Outline each blood parasite and name the species.
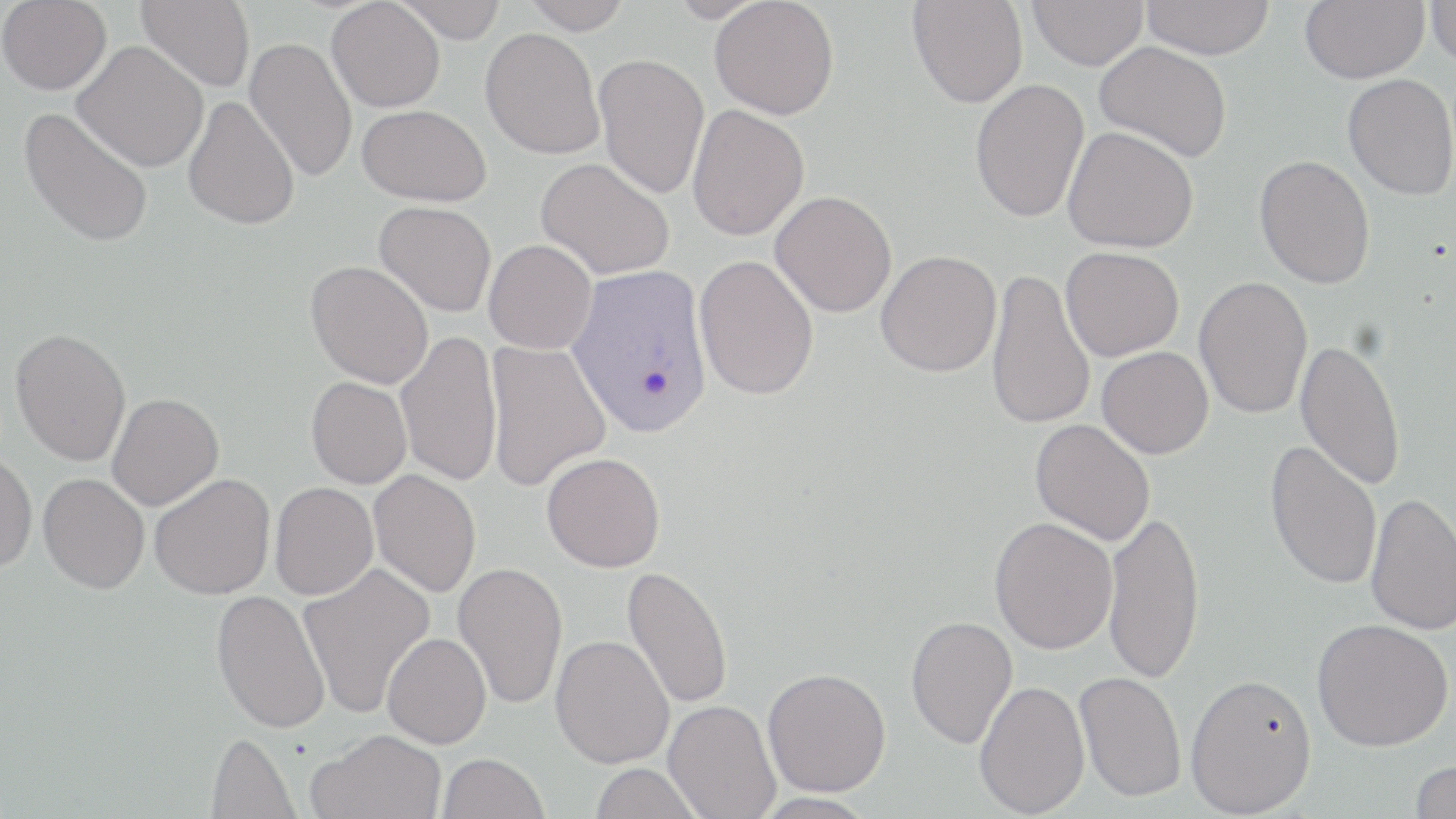

Approximate bounding boxes as (x1, y1, x2, y2) in pixels.
Plasmodium vivax-infected red blood cells: (567, 264, 713, 436).
No Plasmodium falciparum, Plasmodium ovale, Plasmodium malariae, Babesia divergens, or Trypanosoma brucei observed.

Uninfected red blood cell locations: (0, 0, 111, 95), (136, 0, 255, 92), (392, 0, 508, 42), (522, 0, 633, 34), (667, 0, 771, 23), (710, 0, 839, 119), (1028, 0, 1149, 70), (1140, 0, 1275, 59), (1300, 0, 1429, 83), (1425, 0, 1456, 68), (327, 1, 445, 112), (908, 1, 1028, 108), (480, 27, 605, 160), (244, 37, 357, 183), (73, 40, 209, 172), (1094, 42, 1232, 162), (594, 53, 709, 199), (1343, 74, 1456, 200), (970, 79, 1089, 223), (182, 95, 300, 230), (687, 104, 810, 241), (357, 105, 491, 205), (19, 106, 154, 249), (1063, 126, 1199, 253), (1255, 155, 1375, 289), (536, 157, 676, 280), (770, 190, 897, 317), (375, 201, 496, 317), (484, 239, 597, 353), (1061, 247, 1184, 361), (876, 250, 1002, 377), (694, 256, 819, 400), (306, 260, 434, 389), (986, 267, 1096, 431), (1194, 276, 1313, 419), (9, 328, 132, 466), (395, 330, 503, 487), (1294, 337, 1407, 491), (485, 339, 611, 491), (1097, 346, 1214, 459), (306, 377, 412, 489), (107, 393, 224, 510), (1030, 419, 1155, 546), (1265, 439, 1383, 590), (0, 449, 38, 573), (542, 452, 666, 572), (369, 469, 481, 598), (38, 473, 150, 594), (149, 473, 275, 600), (270, 482, 379, 600), (1365, 491, 1456, 635), (1103, 510, 1206, 685), (989, 517, 1118, 654), (452, 561, 568, 710), (297, 562, 435, 719), (622, 565, 734, 709), (211, 589, 330, 733), (905, 615, 1018, 749), (1312, 618, 1454, 752), (382, 633, 491, 748), (550, 634, 674, 768), (763, 667, 891, 796), (1075, 671, 1186, 802), (1185, 672, 1317, 816), (974, 680, 1090, 817), (663, 700, 780, 819), (309, 729, 446, 819), (206, 732, 299, 819), (438, 752, 548, 819), (1408, 758, 1456, 819), (590, 762, 704, 819). Slide-level diagnosis: Plasmodium vivax. Thin blood film. One field of a larger specimen. May-Grünwald-Giemsa stain. Image is 1456×819 pixels. Captured at 1000x magnification. Light microscopy.